Outline each white blood cell.
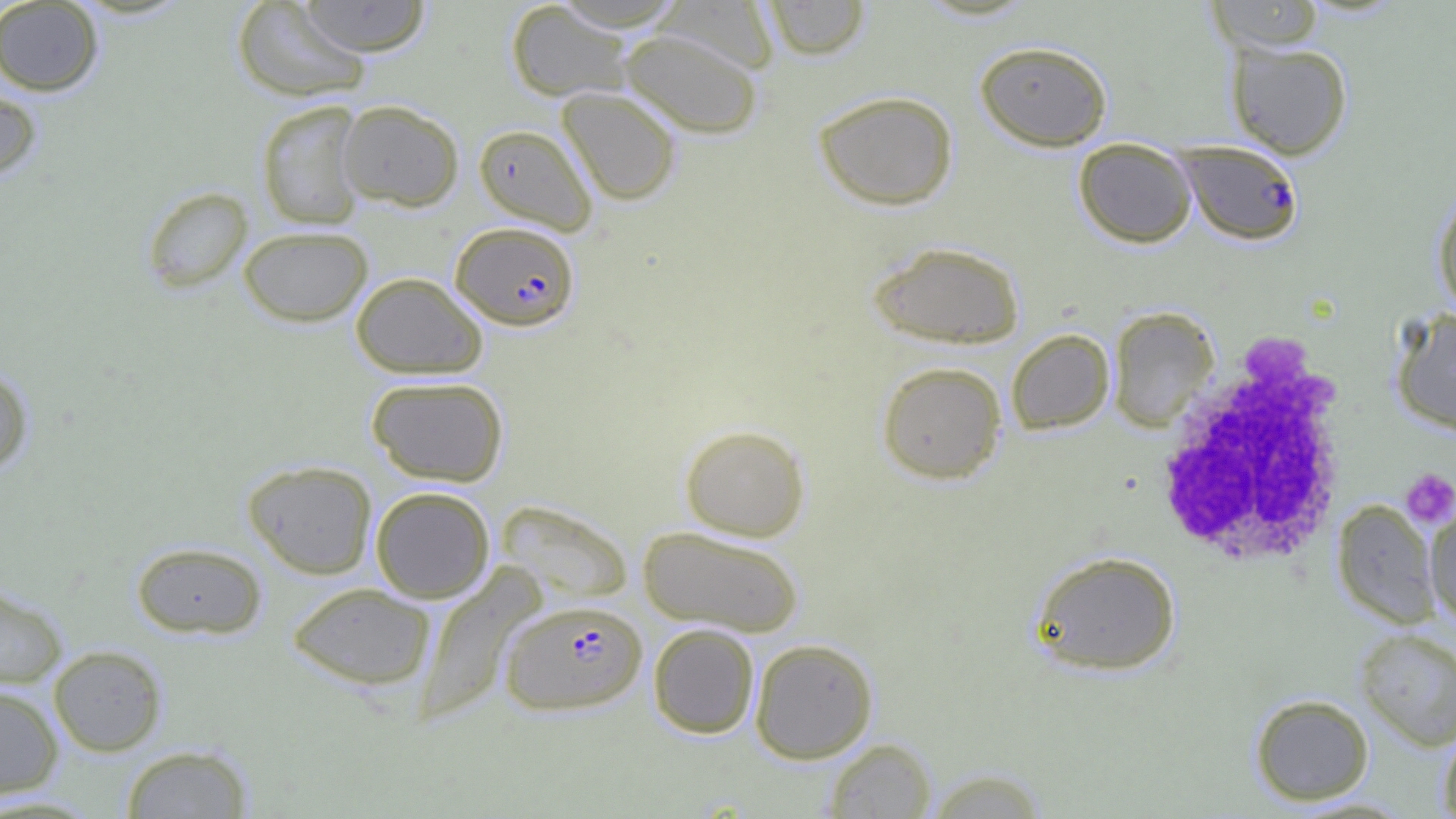

Approximate bounding boxes as [x1, y1, x2, y2] in pixels.
White blood cells: [1152, 335, 1355, 571].

Plasmodium falciparum-infected red blood cell locations: [1177, 141, 1303, 246], [450, 221, 580, 330], [499, 599, 647, 715]. Platelet locations: [1400, 468, 1456, 528]. Uninfected red blood cell locations: [0, 0, 104, 96], [297, 0, 431, 56], [761, 0, 872, 60], [1206, 0, 1325, 52], [231, 1, 372, 102], [505, 1, 635, 102], [656, 1, 780, 74], [619, 29, 763, 139], [975, 40, 1113, 151], [1225, 40, 1353, 159], [0, 78, 43, 183], [557, 87, 682, 205], [813, 90, 959, 211], [256, 100, 367, 230], [337, 100, 464, 211], [473, 123, 599, 235], [1073, 138, 1197, 248], [141, 186, 253, 292], [1432, 187, 1456, 318], [238, 225, 373, 327], [867, 240, 1026, 349], [350, 272, 488, 379], [1108, 306, 1220, 431], [1389, 308, 1456, 435], [1006, 328, 1115, 435], [876, 361, 1007, 484], [0, 365, 34, 474], [366, 376, 509, 486], [680, 424, 811, 541], [242, 459, 377, 579], [370, 486, 496, 602], [495, 498, 633, 605], [1331, 500, 1441, 628], [1425, 502, 1456, 629], [637, 525, 805, 637], [131, 541, 267, 639], [1028, 550, 1182, 677], [0, 582, 68, 688], [286, 582, 437, 691], [648, 623, 760, 739], [1355, 627, 1456, 750], [750, 638, 878, 763], [48, 645, 167, 756], [0, 685, 64, 798], [1249, 693, 1375, 805], [1438, 724, 1456, 818], [824, 737, 936, 818], [120, 744, 254, 818], [923, 767, 1050, 818]. Slide-level diagnosis: Plasmodium falciparum. 1000x magnification. Single field of view. Thin blood film. Image is 1456×819 pixels. Light microscopy.